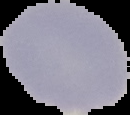
Summary:
  - Malaria status: uninfected
  - Image size: 130×115 pixels
  - Preparation: thin blood smear
  - Image type: segmented cell region with the area outside set to black